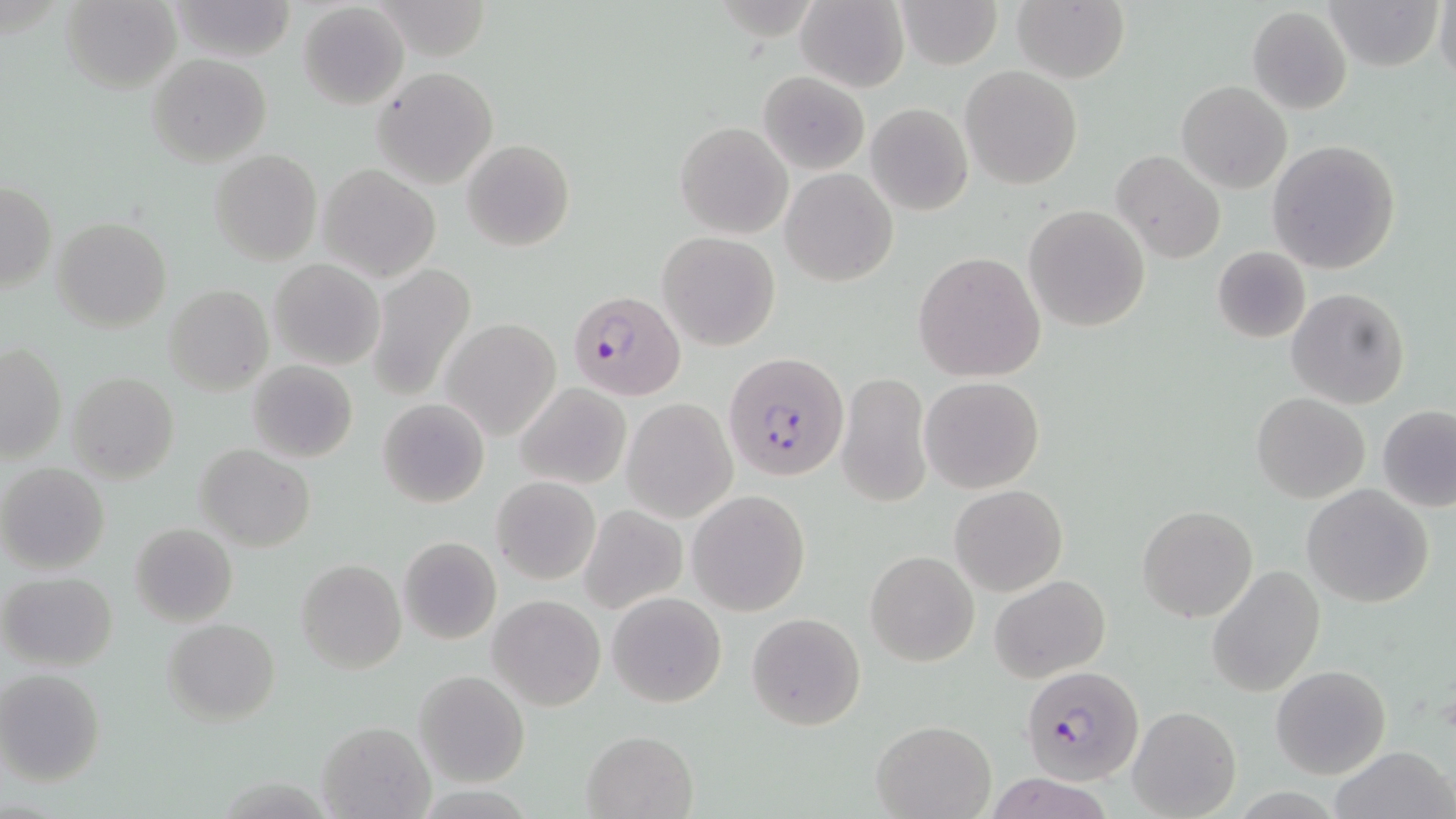
slide_level_diagnosis: Plasmodium falciparum
stain: May-Grünwald-Giemsa
image_size: 1456×819 pixels
magnification: 1000x
uninfected_red_blood_cell_locations: 'approximate bounding boxes as (x1,y1)-(x2,y2) corner pairs in pixels: (61,0)-(182,93), (168,0)-(296,62), (894,0)-(1003,70), (1434,0)-(1456,89), (795,1)-(909,91), (1012,1)-(1130,83), (1321,1)-(1442,72), (297,3)-(408,108), (1246,6)-(1352,114), (146,54)-(272,165), (960,65)-(1083,189), (372,66)-(499,189), (759,72)-(869,174), (1176,80)-(1292,194), (866,103)-(972,215), (675,121)-(793,238), (461,138)-(575,253), (1266,140)-(1401,274), (209,149)-(322,265), (1112,149)-(1225,264), (317,165)-(440,281), (780,167)-(898,287), (1,180)-(55,294), (1023,205)-(1151,331), (53,217)-(171,334), (657,232)-(780,350), (1211,248)-(1311,343), (912,252)-(1046,382), (269,258)-(384,370), (367,265)-(475,400), (163,284)-(273,395), (1287,287)-(1409,409), (441,319)-(562,442), (1,342)-(66,462), (249,360)-(358,463), (837,370)-(932,509), (65,372)-(179,484), (921,376)-(1043,493), (514,383)-(630,489), (1252,393)-(1370,503), (376,398)-(490,508), (622,399)-(737,521), (1378,405)-(1456,511), (194,444)-(316,552), (0,463)-(109,574), (492,476)-(601,587), (951,484)-(1068,596), (1303,484)-(1435,607), (688,490)-(811,616), (1137,504)-(1257,622), (579,505)-(686,614), (896,510)-(1014,646), (130,522)-(238,626), (397,537)-(501,644), (865,550)-(979,665), (296,558)-(406,673), (1207,565)-(1325,698), (2,572)-(117,671), (990,575)-(1110,682), (606,591)-(726,708), (488,594)-(605,711), (746,611)-(867,731), (163,619)-(280,726), (1271,664)-(1391,779), (0,669)-(106,786), (414,670)-(529,788), (1128,705)-(1240,818), (871,719)-(996,819), (316,721)-(433,818), (581,729)-(697,818), (1333,745)-(1452,819)'
field_of_view: single
modality: light microscopy
plasmodium_falciparum_infected_red_blood_cell_locations: 'approximate bounding boxes as (x1,y1)-(x2,y2) corner pairs in pixels: (568,289)-(686,401), (724,352)-(849,483), (1022,663)-(1144,785)'
preparation: thin blood film